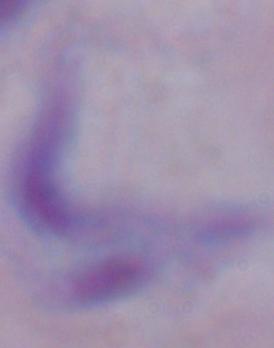
Summary:
  - Identification: trypanosome
  - Modality: photomicrograph
  - Magnification: 1000x